State which parasite is depicted.
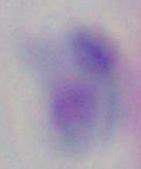
Toxoplasma gondii.

magnification: 1000x
modality: photomicrograph